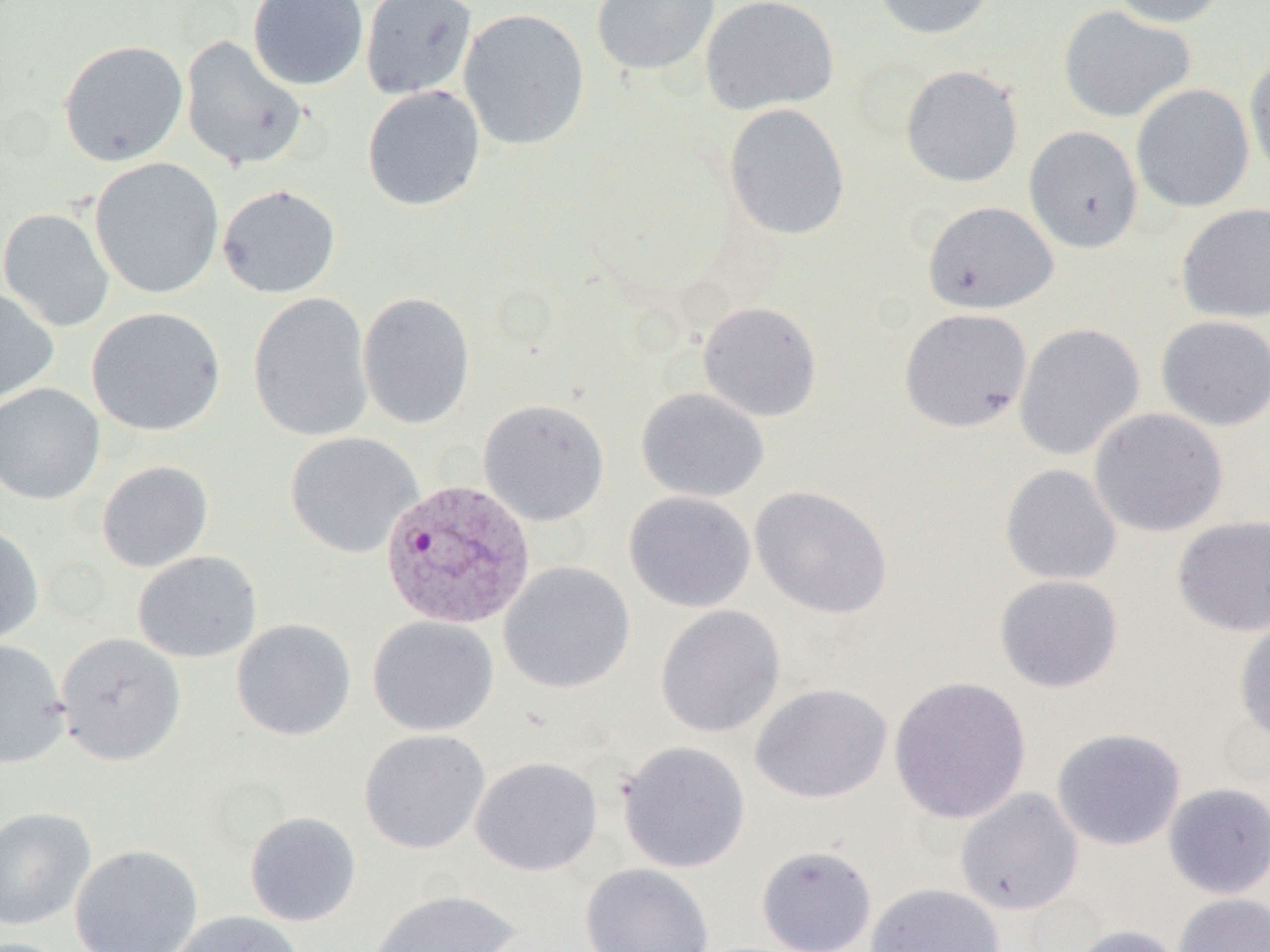
slide-level diagnosis = Plasmodium vivax
magnification = 1000x
uninfected red blood cell locations = approximate bounding boxes as named x1/y1/x2/y2 corners in pixels: (x1=247, y1=0, x2=369, y2=91), (x1=360, y1=0, x2=478, y2=100), (x1=591, y1=0, x2=720, y2=76), (x1=700, y1=0, x2=839, y2=115), (x1=871, y1=0, x2=996, y2=40), (x1=1109, y1=0, x2=1228, y2=28), (x1=1058, y1=5, x2=1196, y2=123), (x1=458, y1=8, x2=591, y2=150), (x1=179, y1=35, x2=310, y2=171), (x1=58, y1=39, x2=189, y2=167), (x1=1244, y1=55, x2=1270, y2=183), (x1=900, y1=65, x2=1023, y2=187), (x1=1131, y1=84, x2=1255, y2=213), (x1=362, y1=85, x2=486, y2=211), (x1=724, y1=103, x2=851, y2=241), (x1=1023, y1=126, x2=1143, y2=253), (x1=89, y1=157, x2=225, y2=299), (x1=217, y1=184, x2=340, y2=298), (x1=922, y1=201, x2=1059, y2=314), (x1=1175, y1=203, x2=1270, y2=323), (x1=0, y1=207, x2=115, y2=332), (x1=0, y1=287, x2=59, y2=406), (x1=249, y1=292, x2=374, y2=443), (x1=357, y1=292, x2=475, y2=430), (x1=698, y1=301, x2=822, y2=421), (x1=86, y1=307, x2=226, y2=436), (x1=899, y1=308, x2=1032, y2=433), (x1=1155, y1=315, x2=1270, y2=431), (x1=1014, y1=323, x2=1145, y2=461), (x1=0, y1=383, x2=105, y2=505), (x1=636, y1=388, x2=770, y2=503), (x1=478, y1=399, x2=610, y2=526), (x1=1089, y1=407, x2=1228, y2=537), (x1=285, y1=432, x2=423, y2=558), (x1=96, y1=461, x2=214, y2=572), (x1=1000, y1=464, x2=1122, y2=586), (x1=750, y1=485, x2=893, y2=619), (x1=623, y1=491, x2=756, y2=612), (x1=1172, y1=515, x2=1270, y2=636), (x1=0, y1=524, x2=45, y2=646), (x1=132, y1=550, x2=263, y2=663), (x1=499, y1=561, x2=635, y2=694), (x1=994, y1=574, x2=1123, y2=693), (x1=655, y1=605, x2=785, y2=738), (x1=367, y1=616, x2=500, y2=736), (x1=1234, y1=617, x2=1270, y2=743), (x1=231, y1=619, x2=356, y2=741), (x1=55, y1=632, x2=186, y2=765), (x1=0, y1=639, x2=69, y2=768), (x1=888, y1=676, x2=1032, y2=824), (x1=751, y1=683, x2=892, y2=803), (x1=1051, y1=727, x2=1186, y2=851), (x1=358, y1=729, x2=491, y2=854), (x1=617, y1=740, x2=751, y2=874), (x1=470, y1=756, x2=603, y2=876), (x1=1163, y1=782, x2=1270, y2=899), (x1=955, y1=787, x2=1084, y2=915), (x1=0, y1=806, x2=96, y2=931), (x1=244, y1=811, x2=362, y2=927), (x1=70, y1=844, x2=203, y2=952), (x1=756, y1=845, x2=877, y2=952), (x1=580, y1=862, x2=714, y2=952), (x1=865, y1=882, x2=1005, y2=952), (x1=368, y1=889, x2=520, y2=952), (x1=1173, y1=893, x2=1269, y2=952), (x1=166, y1=910, x2=305, y2=952), (x1=1068, y1=925, x2=1185, y2=952)
image size = 1270×952 pixels
modality = optical microscopy
preparation = thin blood film
Plasmodium vivax-infected red blood cell locations = approximate bounding boxes as named x1/y1/x2/y2 corners in pixels: (x1=375, y1=477, x2=531, y2=630)
field of view = one of a larger specimen